Name the parasite shown.
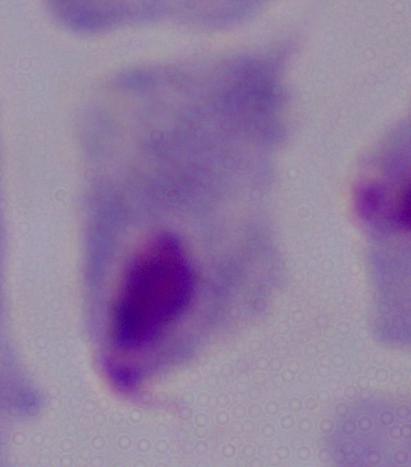

A trichomonad.

magnification: 1000x
modality: micrograph